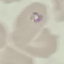

Summary:
  - Malaria status: parasitized
  - Capture: smartphone through the microscope eyepiece
  - Preparation: thin blood film
  - Image type: cell patch, automatically extracted from a larger field of view and resized to 64 × 64 pixels
  - Stain: Giemsa